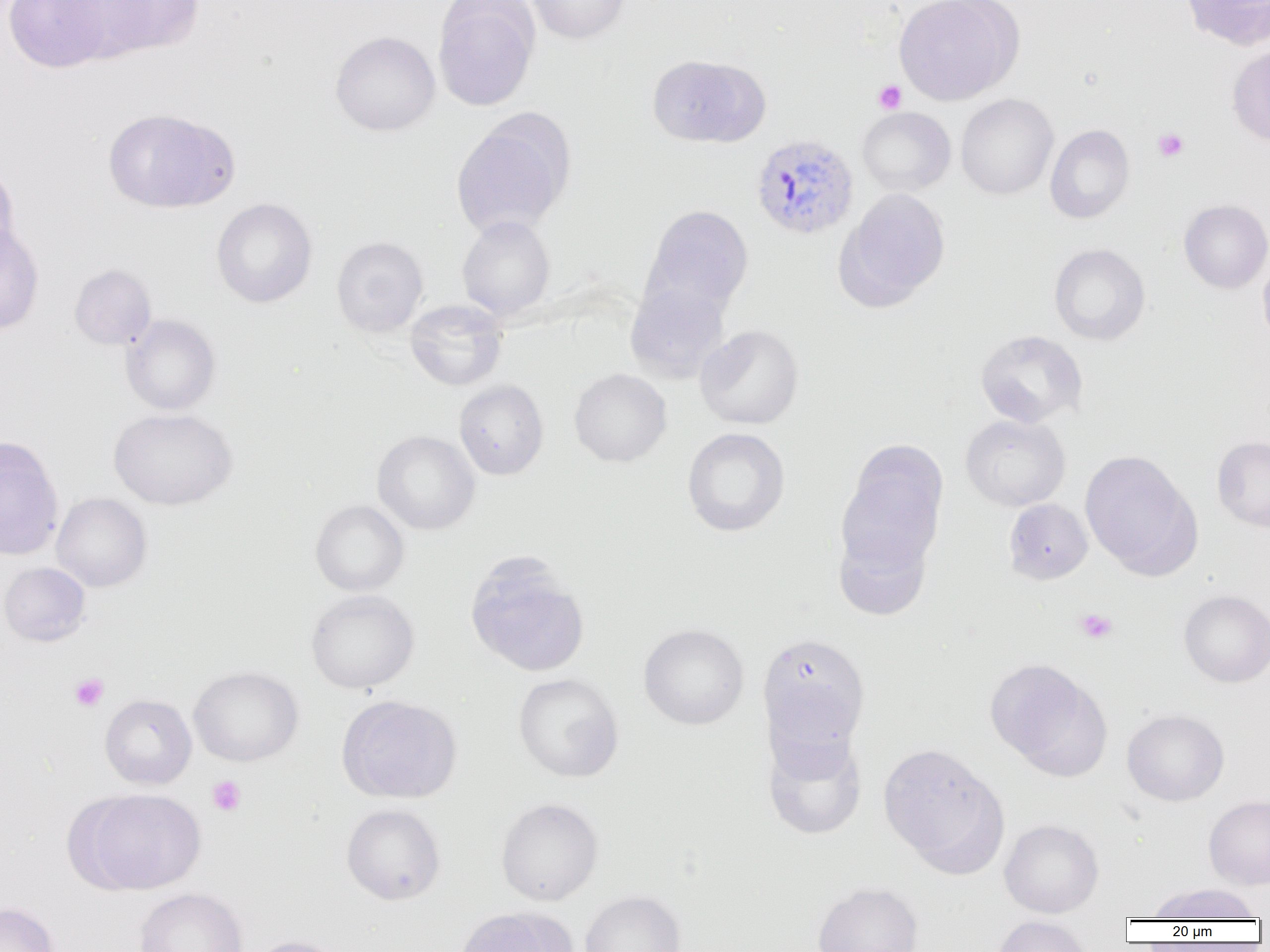
slide_level_diagnosis: Plasmodium vivax
modality: light microscopy
image_size: 1270×952 pixels
platelet_locations: 'approximate bounding boxes as (x1,y1)-(x2,y2) corner pairs in pixels: (873,80)-(906,114), (1152,128)-(1189,162), (1074,608)-(1117,644), (69,673)-(109,711), (207,775)-(246,816)'
field_of_view: one of a larger specimen
magnification: 1000x
plasmodium_vivax_infected_red_blood_cell_locations: 'approximate bounding boxes as (x1,y1)-(x2,y2) corner pairs in pixels: (750,134)-(858,240)'
preparation: thin blood smear
uninfected_red_blood_cell_locations: 'approximate bounding boxes as (x1,y1)-(x2,y2) corner pairs in pixels: (4,0)-(113,73), (81,0)-(205,59), (432,0)-(540,111), (525,0)-(630,44), (893,0)-(1023,105), (1180,0)-(1270,49), (330,30)-(440,136), (1226,44)-(1270,147), (647,54)-(768,148), (956,93)-(1059,200), (857,107)-(956,196), (103,108)-(237,213), (451,117)-(572,238), (1045,124)-(1135,224), (0,164)-(20,266), (836,188)-(951,310), (211,197)-(317,308), (1179,199)-(1270,293), (642,204)-(754,319), (457,215)-(555,321), (0,223)-(44,334), (331,236)-(428,338), (1049,243)-(1151,345), (1257,251)-(1270,350), (69,264)-(156,349), (625,282)-(731,383), (404,299)-(508,391), (120,314)-(221,415), (695,325)-(804,430), (975,330)-(1088,428), (569,368)-(672,467), (454,380)-(549,480), (108,407)-(237,510), (961,414)-(1071,511), (681,427)-(790,537), (372,430)-(480,535), (0,436)-(64,560), (1212,436)-(1270,532), (836,446)-(948,578), (1079,450)-(1199,577), (52,493)-(152,591), (1004,499)-(1093,584), (310,500)-(409,596), (833,526)-(932,621), (464,556)-(591,678), (0,562)-(90,646), (305,589)-(419,694), (1179,590)-(1270,687), (638,623)-(749,730), (757,631)-(870,754), (985,658)-(1110,778), (189,666)-(303,767), (513,673)-(623,783), (100,694)-(197,789), (336,694)-(463,804), (1122,709)-(1229,806), (761,726)-(867,841), (878,743)-(1007,872), (79,788)-(206,894), (1203,794)-(1270,890), (495,797)-(604,906), (341,803)-(445,905), (999,818)-(1104,918), (812,881)-(924,952), (1148,883)-(1260,921), (134,887)-(248,952), (579,890)-(686,952), (0,902)-(59,952), (454,908)-(572,952), (991,915)-(1094,952), (245,935)-(353,952)'